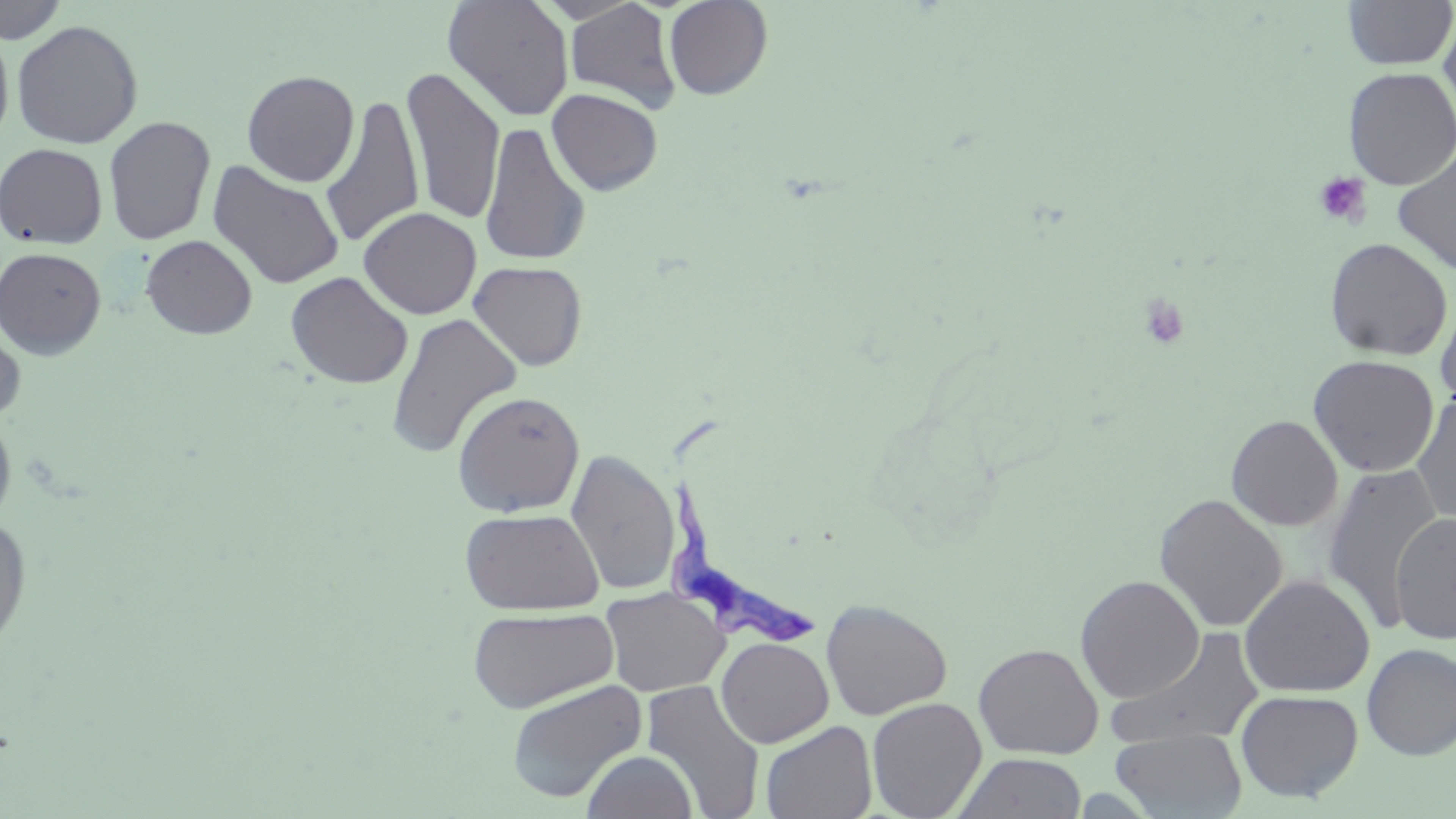
slide-level diagnosis = Trypanosoma brucei
uninfected red blood cell locations = approximate bounding boxes as named x1/y1/x2/y2 corners in pixels: (x1=0, y1=0, x2=68, y2=44), (x1=442, y1=0, x2=575, y2=121), (x1=564, y1=0, x2=681, y2=114), (x1=663, y1=0, x2=772, y2=100), (x1=1342, y1=0, x2=1455, y2=69), (x1=1439, y1=11, x2=1456, y2=126), (x1=11, y1=19, x2=144, y2=149), (x1=0, y1=21, x2=14, y2=147), (x1=402, y1=65, x2=505, y2=227), (x1=1342, y1=67, x2=1456, y2=190), (x1=241, y1=69, x2=360, y2=187), (x1=547, y1=87, x2=663, y2=196), (x1=320, y1=95, x2=425, y2=249), (x1=103, y1=116, x2=216, y2=245), (x1=478, y1=122, x2=591, y2=266), (x1=0, y1=142, x2=108, y2=249), (x1=1393, y1=147, x2=1456, y2=277), (x1=207, y1=161, x2=345, y2=290), (x1=358, y1=207, x2=482, y2=319), (x1=140, y1=234, x2=257, y2=339), (x1=1324, y1=237, x2=1452, y2=360), (x1=0, y1=246, x2=107, y2=359), (x1=468, y1=260, x2=588, y2=371), (x1=286, y1=271, x2=413, y2=389), (x1=1436, y1=294, x2=1456, y2=414), (x1=386, y1=312, x2=522, y2=459), (x1=0, y1=314, x2=26, y2=425), (x1=1308, y1=355, x2=1440, y2=476), (x1=452, y1=390, x2=585, y2=518), (x1=1411, y1=394, x2=1456, y2=527), (x1=0, y1=410, x2=17, y2=529), (x1=1226, y1=415, x2=1343, y2=531), (x1=566, y1=449, x2=679, y2=598), (x1=1322, y1=463, x2=1444, y2=631), (x1=1154, y1=492, x2=1288, y2=632), (x1=459, y1=507, x2=603, y2=615), (x1=1390, y1=511, x2=1456, y2=643), (x1=0, y1=514, x2=33, y2=654), (x1=1239, y1=574, x2=1375, y2=697), (x1=1075, y1=575, x2=1205, y2=703), (x1=600, y1=587, x2=729, y2=697), (x1=821, y1=599, x2=952, y2=720), (x1=467, y1=606, x2=618, y2=714), (x1=1108, y1=628, x2=1266, y2=749), (x1=716, y1=637, x2=834, y2=748), (x1=973, y1=643, x2=1104, y2=759), (x1=1362, y1=644, x2=1456, y2=760), (x1=506, y1=678, x2=647, y2=803), (x1=641, y1=680, x2=765, y2=819), (x1=1235, y1=689, x2=1364, y2=802), (x1=866, y1=696, x2=987, y2=818), (x1=760, y1=720, x2=877, y2=819), (x1=1111, y1=727, x2=1247, y2=818), (x1=582, y1=750, x2=698, y2=819), (x1=953, y1=752, x2=1087, y2=818)
modality = light microscopy
Trypanosoma brucei locations = approximate bounding boxes as named x1/y1/x2/y2 corners in pixels: (x1=660, y1=423, x2=826, y2=653)
platelet locations = approximate bounding boxes as named x1/y1/x2/y2 corners in pixels: (x1=1313, y1=172, x2=1372, y2=226), (x1=1138, y1=295, x2=1192, y2=351)
stain = May-Grünwald-Giemsa
image size = 1456×819 pixels
magnification = 1000x
preparation = thin blood film
field of view = single